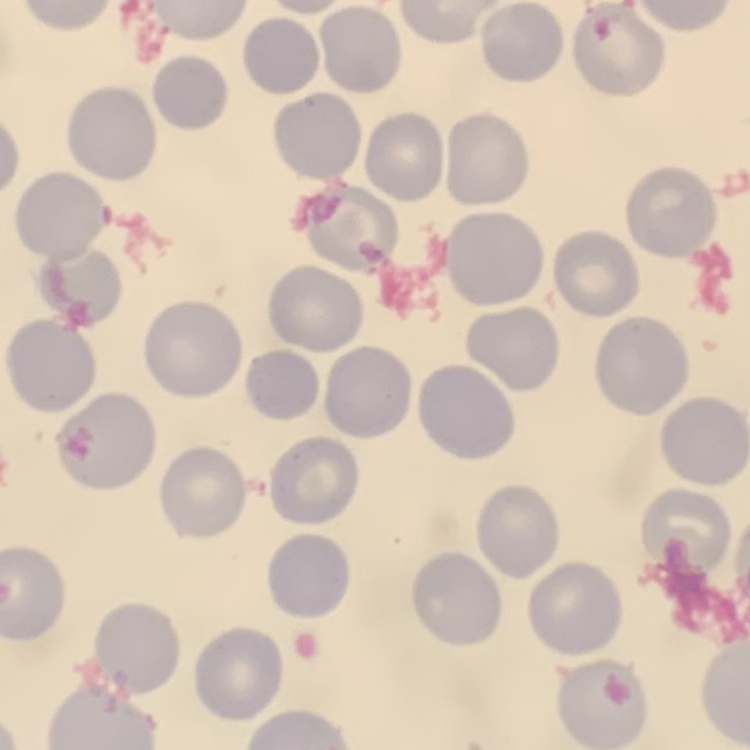

Summary:
  - Erythrocyte morphology: no rouleaux formation
  - Preparation: thin blood film
  - Stain: Field's or Giemsa
  - Image type: square crop of a larger photomicrograph